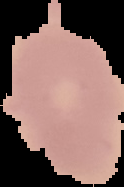

image_size: 124×187 pixels
preparation: thin blood film
malaria_status: uninfected
image_type: segmented cell region with the area outside set to black